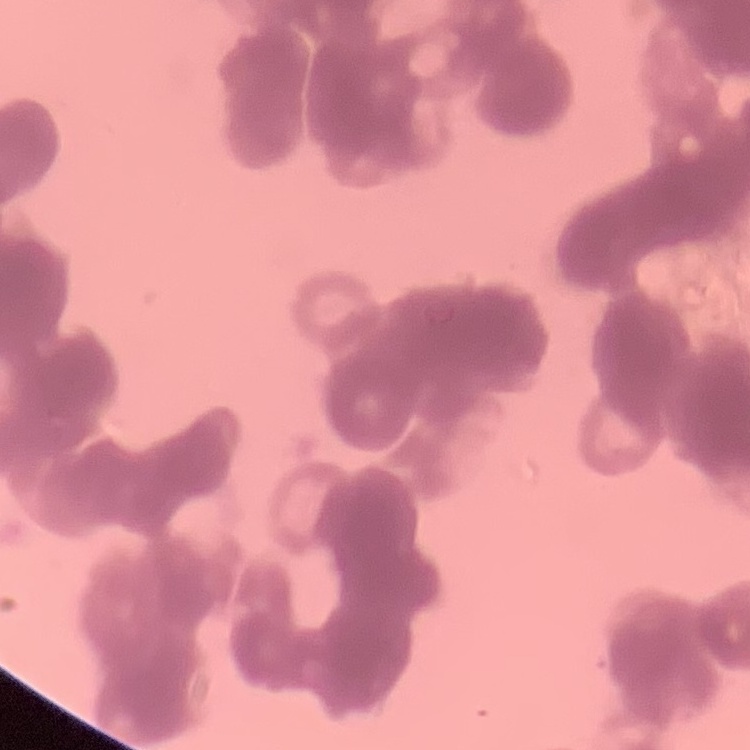

erythrocyte morphology = rouleaux formation
stain = Field's or Giemsa
image type = one tile cut from a larger photomicrograph
preparation = thin blood smear